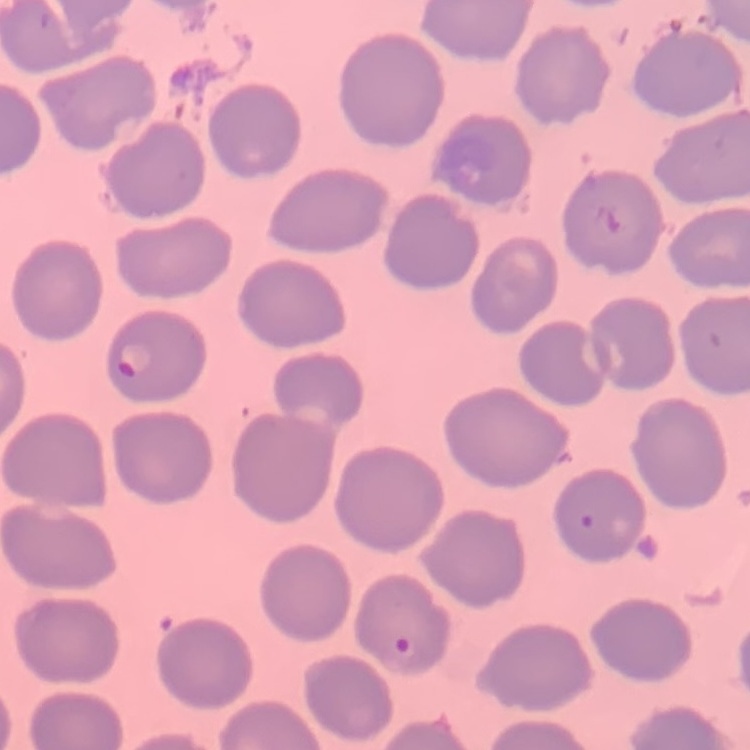

red blood cell morphology = no rouleaux formation
stain = Field's or Giemsa
image type = square crop of a larger photomicrograph
preparation = thin blood film